Identify the cell.
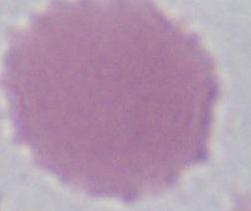
An erythrocyte.

Photomicrograph. Captured at 1000x magnification.